Locate every blood parasite and identify its species.
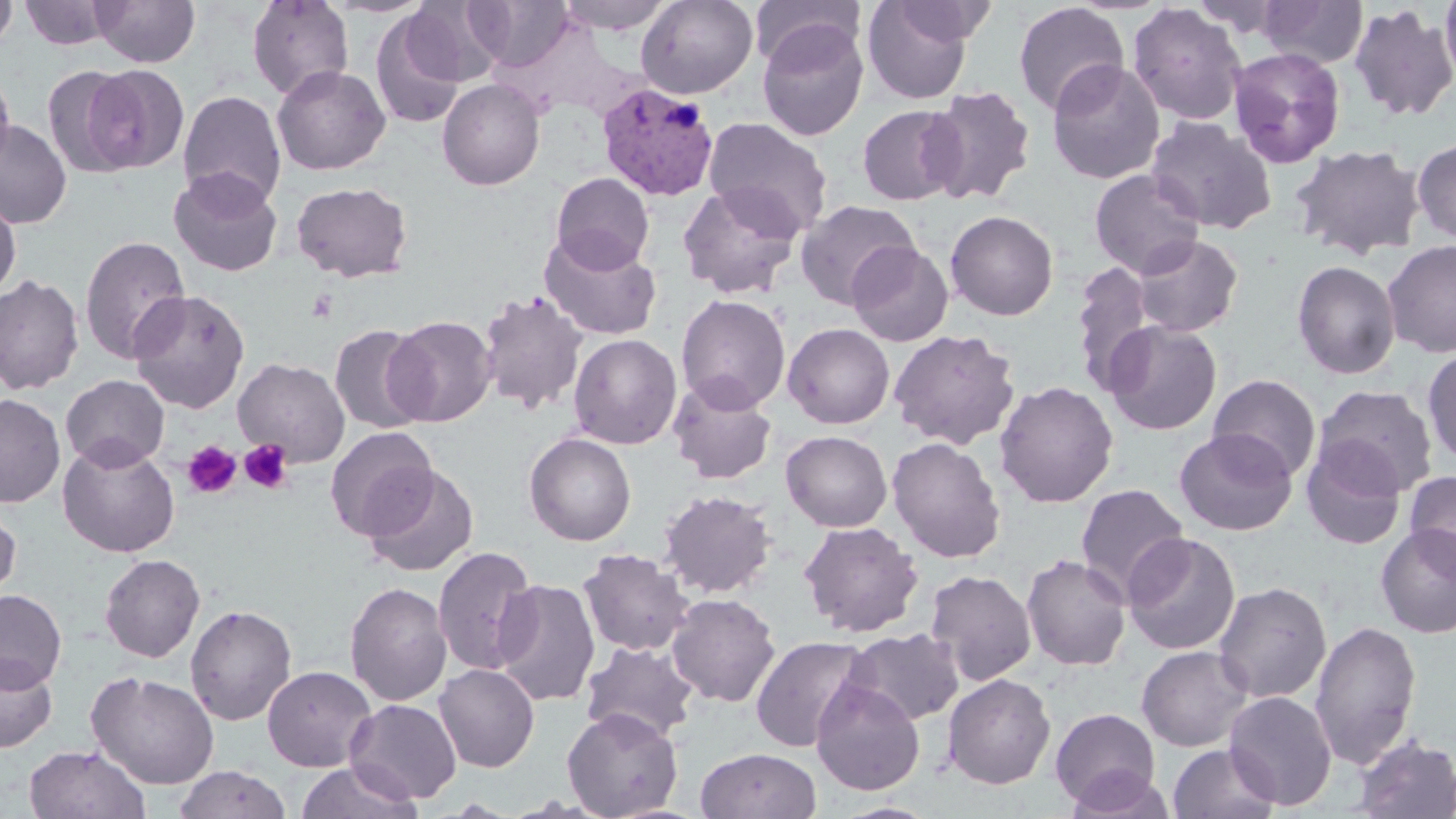

Approximate bounding boxes as (x1, y1, x2, y2) in pixels.
Plasmodium vivax-infected red blood cells: (596, 83, 719, 202).
No Plasmodium falciparum, Plasmodium ovale, Plasmodium malariae, Babesia divergens, or Trypanosoma brucei observed.

slide-level diagnosis = Plasmodium vivax
platelet locations = approximate bounding boxes as (x1, y1, x2, y2) in pixels: (239, 439, 292, 494), (183, 440, 242, 499)
preparation = thin blood film
magnification = 1000x
uninfected red blood cell locations = approximate bounding boxes as (x1, y1, x2, y2) in pixels: (90, 0, 200, 67), (247, 0, 354, 100), (555, 0, 677, 34), (636, 0, 758, 99), (862, 0, 977, 104), (889, 0, 998, 46), (1258, 0, 1368, 68), (1440, 0, 1456, 90), (0, 1, 18, 53), (20, 1, 115, 50), (401, 1, 503, 87), (751, 1, 864, 71), (1013, 2, 1129, 116), (1127, 2, 1248, 125), (1348, 3, 1456, 122), (369, 12, 467, 129), (757, 20, 869, 142), (1228, 47, 1345, 168), (1046, 59, 1165, 185), (1, 64, 15, 174), (82, 64, 189, 174), (43, 65, 141, 177), (272, 65, 391, 176), (437, 78, 545, 191), (922, 85, 1037, 206), (178, 89, 286, 209), (857, 104, 965, 206), (702, 116, 833, 238), (1145, 116, 1276, 234), (1, 118, 72, 228), (1412, 138, 1456, 244), (1289, 143, 1426, 261), (168, 167, 283, 276), (1089, 168, 1206, 279), (551, 172, 654, 273), (291, 181, 413, 282), (677, 182, 804, 299), (0, 194, 21, 300), (795, 199, 921, 309), (945, 209, 1059, 320), (539, 229, 661, 341), (79, 234, 191, 364), (1131, 234, 1244, 338), (1382, 240, 1456, 357), (846, 241, 953, 346), (1292, 260, 1401, 380), (1070, 261, 1156, 395), (0, 273, 84, 395), (129, 289, 250, 413), (476, 289, 588, 414), (676, 294, 791, 412), (386, 315, 496, 427), (1102, 319, 1222, 435), (783, 323, 895, 429), (330, 324, 431, 434), (888, 328, 1020, 450), (568, 333, 682, 449), (1422, 347, 1456, 469), (233, 357, 350, 467), (60, 374, 170, 472), (1208, 374, 1322, 482), (667, 376, 777, 484), (993, 380, 1119, 508), (1313, 385, 1439, 497), (0, 393, 66, 508), (325, 426, 438, 540), (1174, 428, 1297, 536), (781, 430, 892, 531), (524, 433, 636, 545), (887, 437, 1006, 563), (1300, 437, 1408, 550), (57, 438, 180, 558), (364, 465, 479, 576), (1404, 470, 1456, 578), (1075, 483, 1190, 603), (659, 489, 776, 598), (0, 505, 22, 605), (798, 520, 924, 637), (1375, 524, 1456, 639), (1122, 533, 1242, 654), (432, 545, 538, 676), (578, 548, 694, 656), (1021, 553, 1132, 671), (99, 554, 205, 663), (924, 569, 1037, 687), (492, 579, 601, 707), (345, 581, 452, 706), (1212, 581, 1332, 703), (0, 589, 67, 691), (666, 593, 781, 707), (185, 604, 297, 725), (1310, 620, 1421, 768), (843, 627, 965, 726), (750, 634, 871, 752), (580, 640, 700, 744), (1136, 645, 1253, 751), (0, 652, 58, 752), (433, 663, 540, 772), (262, 665, 377, 771), (86, 670, 220, 789), (941, 673, 1056, 789), (810, 677, 926, 796), (1224, 690, 1338, 810), (345, 698, 462, 803), (562, 707, 684, 818), (1050, 707, 1161, 811), (1351, 734, 1456, 818), (1168, 742, 1280, 819), (23, 744, 150, 819), (695, 748, 822, 819), (294, 761, 423, 819), (172, 765, 293, 819), (1064, 767, 1177, 818), (832, 802, 940, 819)
modality = light microscopy
image size = 1456×819 pixels
stain = May-Grünwald-Giemsa
field of view = one of a larger specimen